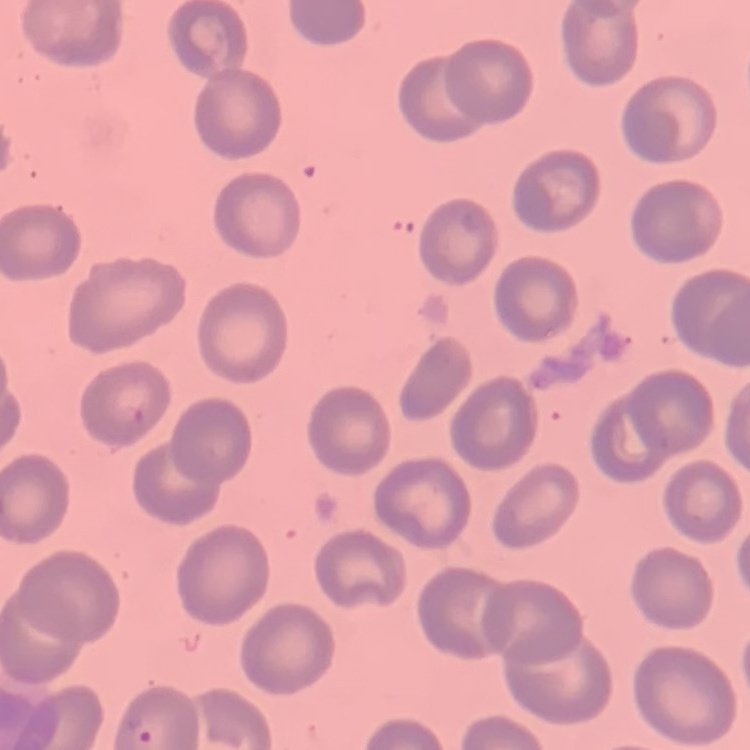 The red blood cells exhibit no rouleaux formation. Thin peripheral smear. Field's or Giemsa stain. Square crop of a larger photomicrograph.